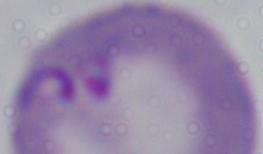
Micrograph. 1000x magnification. A Babesia parasite is shown.